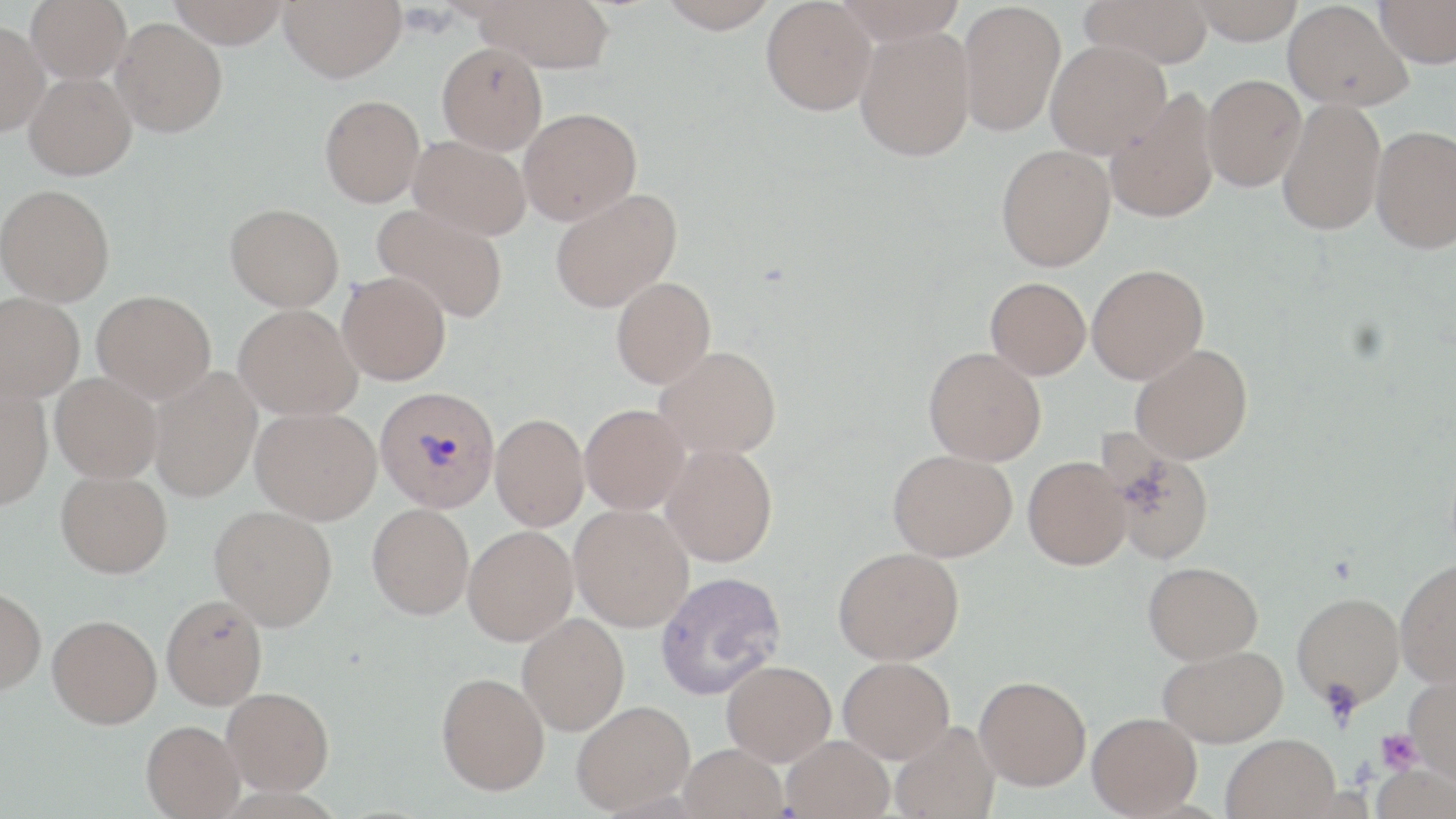
slide_level_diagnosis: Plasmodium vivax
uninfected_red_blood_cell_locations: 'approximate bounding boxes as (x1, y1, x2, y2) in pixels: (26, 0, 131, 83), (167, 0, 290, 48), (279, 0, 406, 82), (475, 0, 614, 72), (659, 0, 778, 34), (761, 0, 876, 115), (835, 0, 968, 44), (1080, 0, 1213, 69), (1191, 0, 1304, 43), (1374, 0, 1456, 67), (1283, 1, 1413, 111), (958, 2, 1065, 136), (110, 18, 227, 137), (0, 21, 50, 137), (855, 26, 976, 161), (1046, 39, 1171, 158), (437, 42, 547, 154), (25, 72, 136, 179), (1202, 74, 1306, 192), (1104, 89, 1219, 224), (320, 95, 424, 207), (1277, 98, 1386, 236), (518, 107, 642, 225), (1370, 125, 1456, 253), (409, 136, 531, 239), (996, 144, 1115, 271), (0, 184, 115, 305), (550, 188, 682, 313), (225, 203, 344, 311), (372, 205, 508, 323), (1087, 263, 1208, 384), (337, 271, 451, 385), (985, 276, 1091, 379), (611, 277, 716, 388), (92, 290, 216, 403), (0, 292, 85, 402), (233, 304, 361, 419), (1131, 343, 1253, 464), (655, 346, 782, 459), (923, 346, 1046, 465), (149, 366, 262, 502), (50, 372, 162, 482), (0, 384, 52, 509), (580, 403, 689, 514), (251, 406, 381, 524), (490, 413, 589, 530), (1103, 438, 1216, 565), (662, 443, 778, 566), (888, 449, 1017, 561), (1023, 455, 1132, 570), (56, 469, 172, 578), (367, 503, 473, 619), (569, 504, 694, 631), (210, 505, 337, 630), (463, 525, 578, 645), (833, 546, 964, 665), (1395, 558, 1456, 687), (1143, 561, 1263, 664), (655, 570, 786, 699), (0, 586, 46, 694), (1292, 591, 1405, 709), (161, 594, 268, 710), (517, 613, 629, 735), (47, 614, 162, 728), (1158, 644, 1288, 747), (838, 657, 955, 763), (722, 660, 836, 765), (436, 672, 550, 795), (1405, 673, 1456, 785), (975, 675, 1091, 789), (222, 687, 334, 795), (571, 700, 695, 814), (1087, 712, 1202, 817), (141, 720, 244, 818), (889, 721, 1000, 819), (1221, 734, 1340, 819), (781, 735, 894, 819), (679, 744, 788, 819)'
preparation: thin blood smear
field_of_view: one of a larger specimen
plasmodium_vivax_infected_red_blood_cell_locations: 'approximate bounding boxes as (x1, y1, x2, y2) in pixels: (374, 386, 500, 513)'
modality: optical microscopy
stain: May-Grünwald-Giemsa
image_size: 1456×819 pixels
platelet_locations: 'approximate bounding boxes as (x1, y1, x2, y2) in pixels: (1323, 683, 1362, 729), (1375, 728, 1423, 774)'
magnification: 1000x